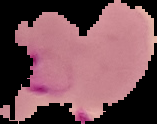
Malaria status: parasitized. Segmented cell region on a black background. From a thin blood smear. Image is 157×124 pixels.